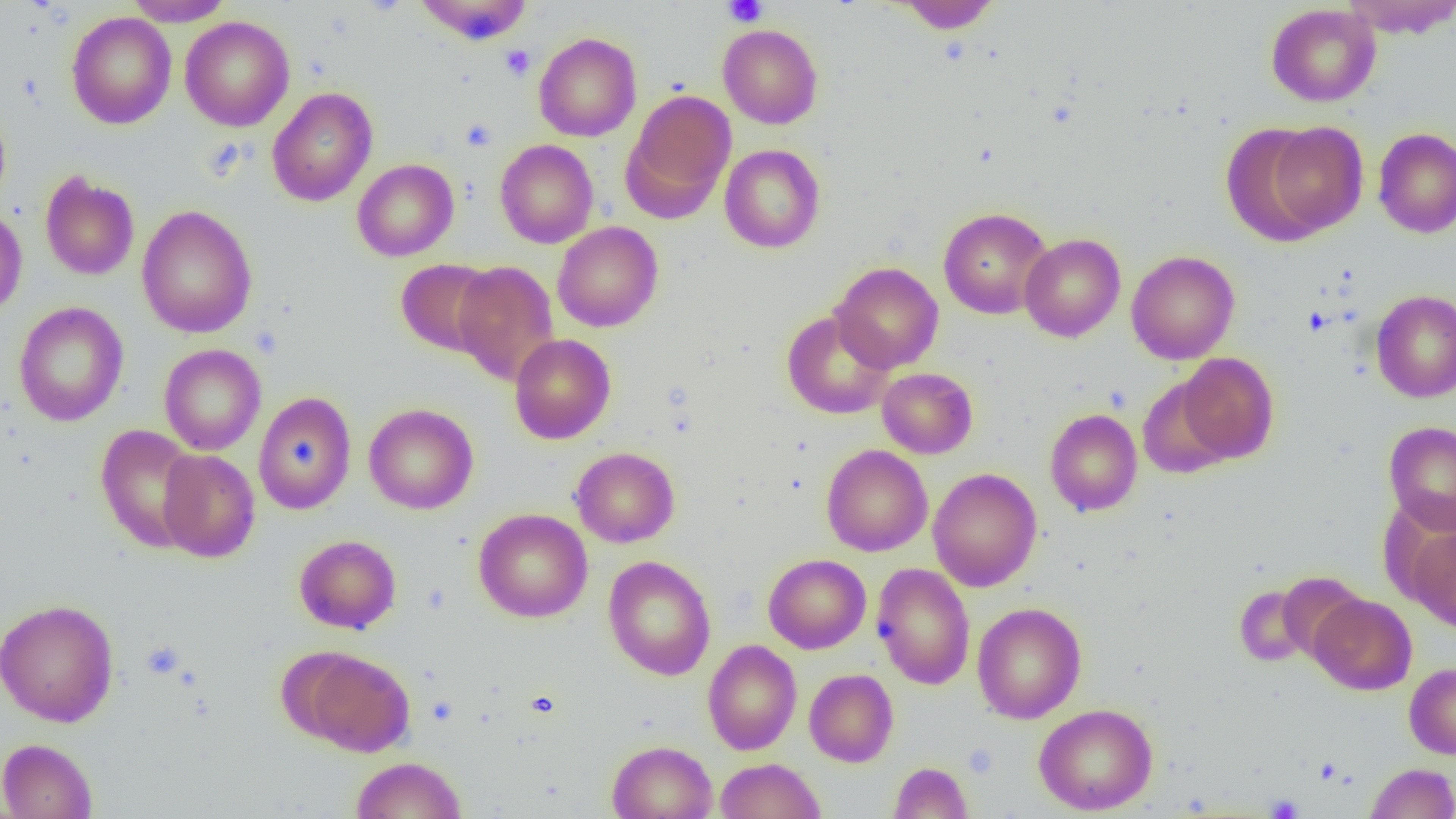 Approximate bounding boxes as [x1, y1, x2, y2] in pixels. Uninfected red blood cell locations: [124, 0, 233, 26], [896, 0, 1001, 32], [1341, 0, 1456, 38], [413, 1, 534, 45], [1266, 4, 1381, 107], [66, 11, 176, 129], [180, 15, 295, 131], [718, 24, 823, 129], [533, 32, 642, 142], [266, 87, 378, 206], [621, 89, 736, 219], [0, 102, 12, 212], [1261, 121, 1369, 237], [1221, 123, 1332, 246], [1372, 127, 1456, 238], [495, 140, 598, 248], [719, 144, 825, 253], [352, 159, 459, 261], [40, 172, 139, 281], [137, 204, 257, 338], [938, 207, 1053, 319], [0, 208, 27, 319], [552, 221, 663, 332], [1019, 233, 1126, 342], [1126, 250, 1240, 364], [396, 259, 499, 356], [452, 261, 560, 386], [831, 262, 944, 373], [1370, 289, 1456, 403], [13, 301, 129, 426], [781, 309, 895, 419], [509, 334, 616, 444], [159, 344, 266, 455], [1177, 353, 1279, 463], [877, 367, 978, 459], [1136, 377, 1236, 478], [253, 391, 356, 514], [363, 403, 479, 515], [1045, 409, 1142, 516], [1384, 420, 1456, 534], [94, 424, 203, 553], [821, 444, 932, 556], [571, 447, 679, 547], [158, 449, 260, 562], [927, 468, 1041, 591], [473, 508, 593, 623], [1406, 526, 1456, 632], [294, 534, 401, 634], [763, 553, 871, 654], [602, 555, 716, 680], [872, 562, 975, 689], [1233, 583, 1316, 667], [1309, 593, 1417, 695], [0, 598, 118, 727], [972, 602, 1087, 723], [703, 639, 802, 755], [298, 649, 415, 756], [1404, 662, 1456, 759], [805, 669, 899, 767], [1033, 703, 1158, 815], [0, 738, 98, 819], [607, 740, 717, 819], [350, 756, 467, 818], [715, 758, 825, 818], [888, 761, 973, 819], [1365, 763, 1456, 819]. Platelet locations: [723, 0, 768, 26], [499, 44, 535, 80], [461, 118, 498, 151], [1304, 308, 1331, 336], [141, 641, 185, 679], [1266, 794, 1305, 818]. Slide-level diagnosis: no evidence of blood parasites. Captured at 1000x magnification. Light microscopy. Image is 1456×819 pixels. Thin blood film. One field of a larger specimen.